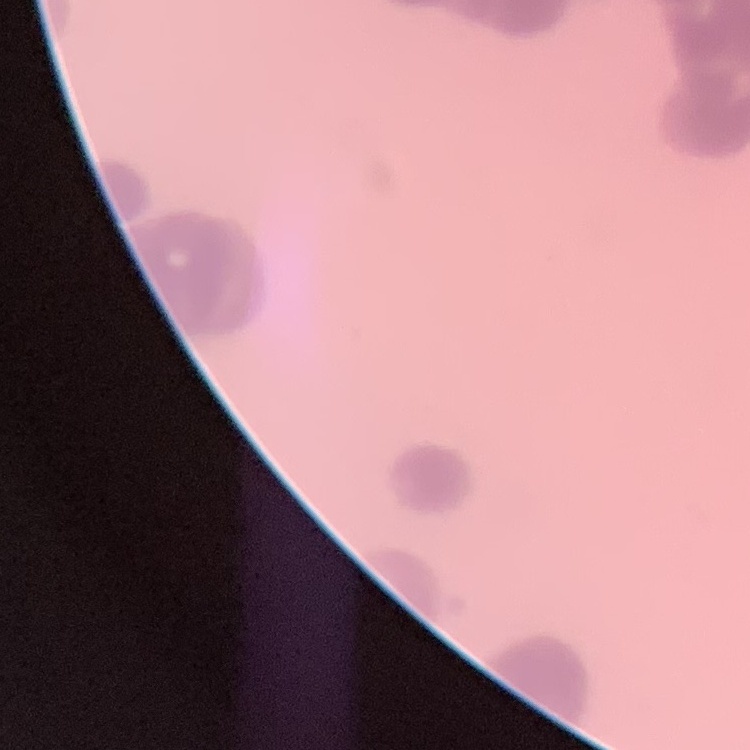
Summary:
  - Red blood cell morphology: rouleaux formation
  - Stain: Field's or Giemsa
  - Preparation: thin peripheral smear
  - Image type: one tile cut from a larger photomicrograph